Assess the morphology of the red blood cells.
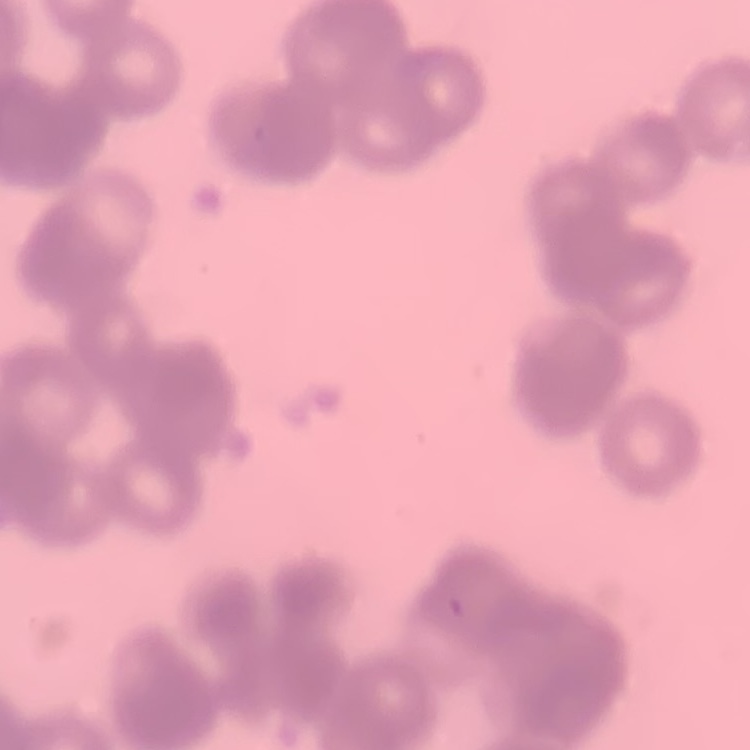
Rouleaux formation.

Summary:
  - Preparation: thin peripheral smear
  - Image type: square crop of a larger photomicrograph
  - Stain: Field's or Giemsa